State which parasite is depicted.
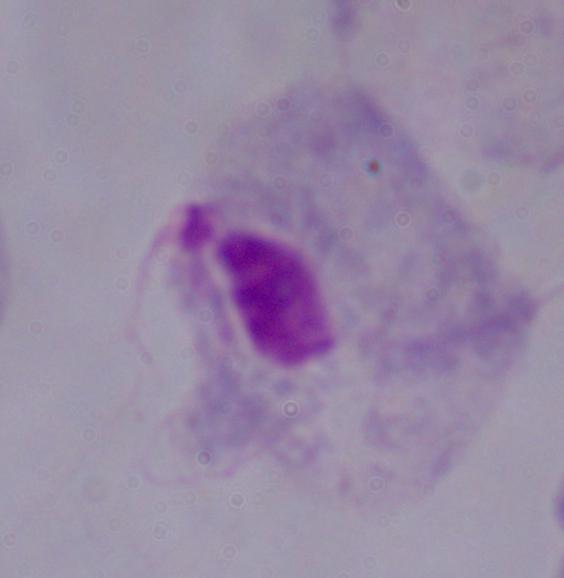
A trichomonad.

{
  "magnification": "1000x",
  "modality": "photomicrograph"
}